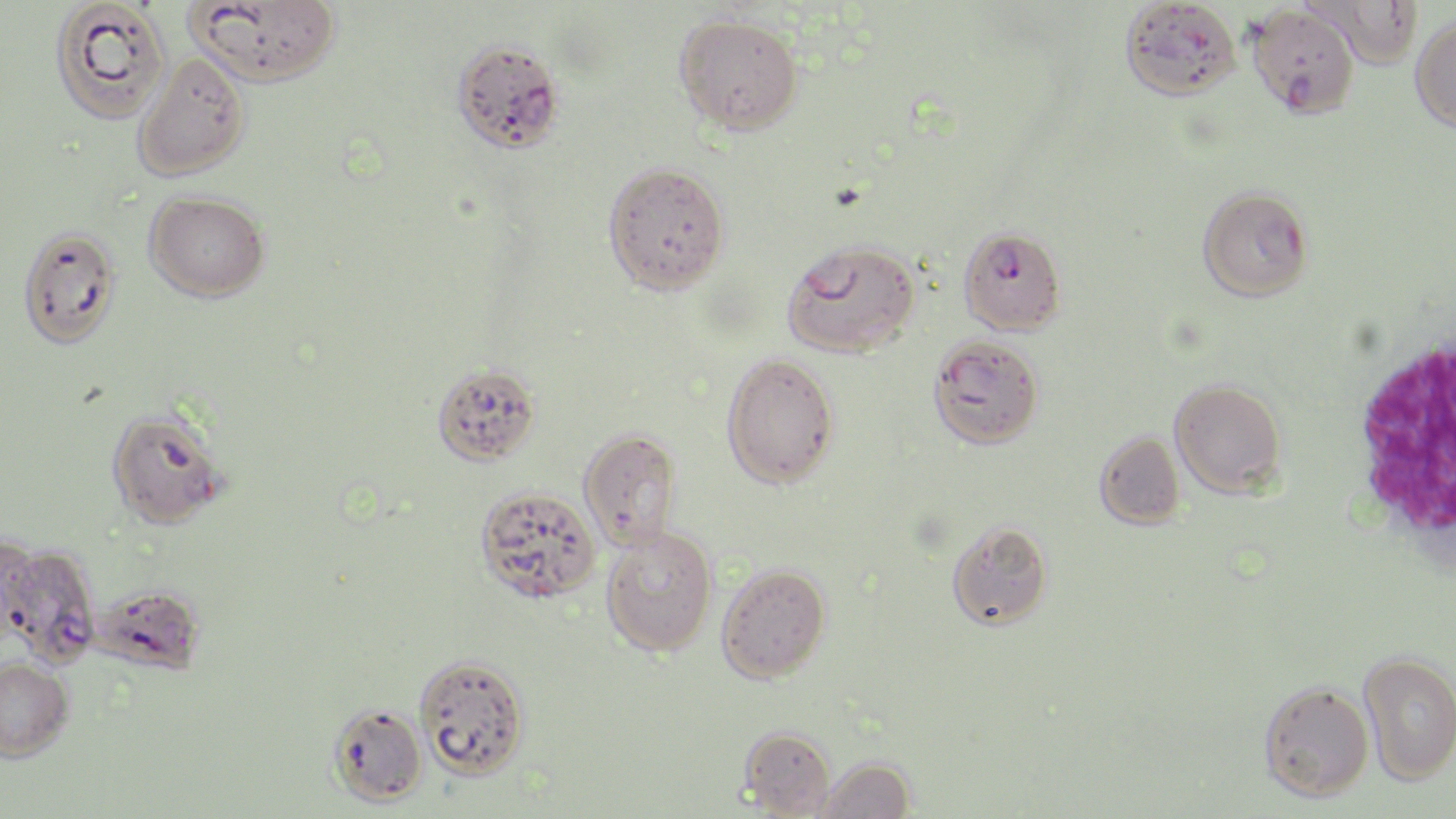
slide-level diagnosis = Plasmodium falciparum
field of view = one of a larger specimen
Plasmodium falciparum-infected red blood cell locations = approximate bounding boxes as (x1,y1)-(x2,y2) corner pairs in pixels: (958,226)-(1066,336), (1,541)-(102,667)
magnification = 1000x
image size = 1456×819 pixels
modality = light microscopy
white blood cell locations = approximate bounding boxes as (x1,y1)-(x2,y2) corner pairs in pixels: (1344,324)-(1456,572)
preparation = thin blood smear
stain = May-Grünwald-Giemsa
uninfected red blood cell locations = approximate bounding boxes as (x1,y1)-(x2,y2) corner pairs in pixels: (48,0)-(172,124), (188,0)-(342,88), (1120,0)-(1241,101), (1307,1)-(1423,70), (1248,4)-(1359,118), (674,14)-(803,136), (1410,15)-(1456,133), (451,38)-(564,155), (132,54)-(251,181), (602,161)-(730,295), (1197,185)-(1314,302), (144,190)-(270,302), (17,225)-(122,349), (782,239)-(920,359), (927,336)-(1043,450), (721,352)-(840,489), (431,363)-(541,467), (1169,379)-(1287,498), (105,406)-(228,529), (578,429)-(683,550), (1094,431)-(1186,530), (474,484)-(600,603), (946,520)-(1053,630), (601,527)-(717,656), (716,563)-(831,683), (82,584)-(207,672), (1358,651)-(1456,785), (414,653)-(531,778), (0,656)-(74,762), (1258,681)-(1374,802), (328,703)-(427,806), (738,726)-(837,817), (815,756)-(915,818)